Classify this cell by malaria status.
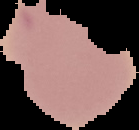
It is uninfected.

From a thin blood smear. The area outside the segmented cell region is set to black. Image is 139×130 pixels.